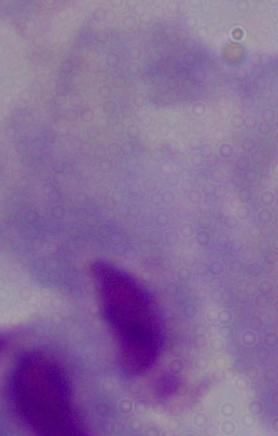 Micrograph. 1000x magnification. A trichomonad is seen.